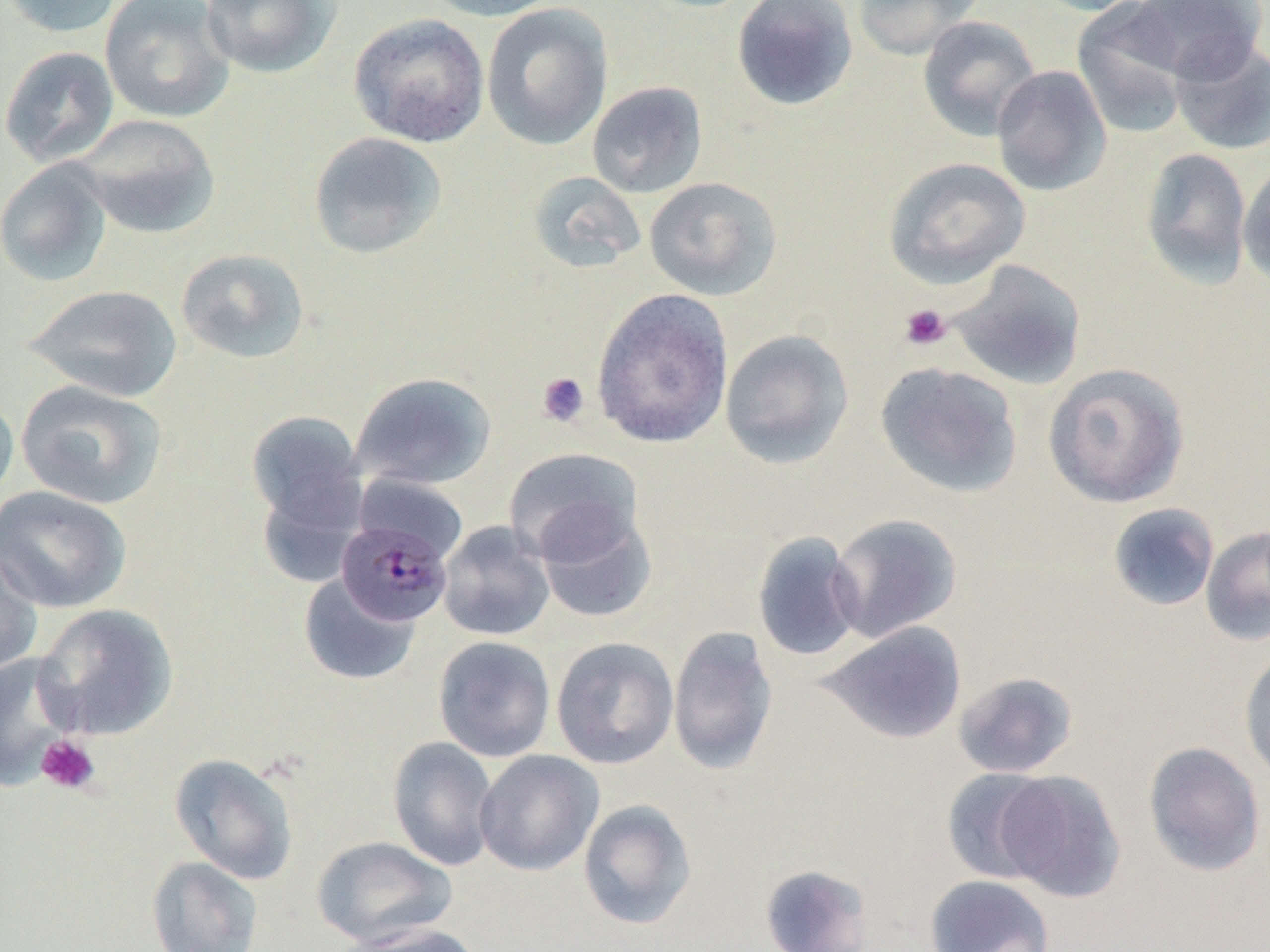

slide_level_diagnosis: Plasmodium malariae
preparation: thin blood film
platelet_locations: 'approximate bounding boxes as (x1,y1)-(x2,y2) corner pairs in pixels: (899,303)-(952,351), (536,371)-(590,427), (36,735)-(100,795)'
uninfected_red_blood_cell_locations: 'approximate bounding boxes as (x1,y1)-(x2,y2) corner pairs in pixels: (1,0)-(124,38), (99,0)-(235,124), (199,0)-(341,79), (421,0)-(567,22), (731,0)-(859,111), (851,0)-(985,60), (1027,0)-(1153,16), (1128,0)-(1266,83), (1071,2)-(1193,138), (481,3)-(613,151), (348,13)-(490,148), (917,15)-(1041,141), (1169,38)-(1270,155), (0,45)-(119,168), (991,65)-(1112,197), (587,81)-(707,199), (74,114)-(222,239), (308,131)-(447,260), (1140,147)-(1253,289), (883,157)-(1030,289), (0,159)-(113,287), (1238,159)-(1270,290), (527,171)-(646,274), (644,176)-(783,301), (175,248)-(310,364), (948,259)-(1086,390), (24,283)-(182,402), (591,288)-(734,449), (719,329)-(855,469), (874,361)-(1022,499), (1042,362)-(1190,508), (350,372)-(497,490), (15,380)-(167,510), (0,389)-(19,510), (246,410)-(366,532), (503,447)-(642,564), (358,470)-(475,556), (1,485)-(132,614), (1107,502)-(1220,612), (535,506)-(657,624), (828,513)-(962,642), (437,521)-(555,641), (1201,525)-(1270,647), (751,531)-(864,662), (0,543)-(44,677), (298,573)-(420,686), (33,603)-(178,740), (820,621)-(967,744), (668,626)-(778,775), (432,635)-(556,762), (551,637)-(679,769), (1238,648)-(1270,784), (0,651)-(80,789), (952,670)-(1079,779), (387,736)-(499,871), (1143,741)-(1266,877), (474,749)-(604,876), (169,752)-(299,885), (941,768)-(1059,884), (994,770)-(1126,903), (578,799)-(696,930), (311,836)-(459,948), (146,856)-(264,952), (759,864)-(874,952), (924,874)-(1055,952), (342,923)-(483,952)'
modality: light microscopy
magnification: 1000x
image_size: 1270×952 pixels
plasmodium_malariae_infected_red_blood_cell_locations: 'approximate bounding boxes as (x1,y1)-(x2,y2) corner pairs in pixels: (335,516)-(454,630)'
field_of_view: single